Report the malaria status of this cell.
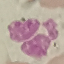

Uninfected.

Cell patch, automatically extracted from a larger field of view and resized to 64 × 64 pixels. Thin blood smear. Acquired by smartphone through the microscope eyepiece. Giemsa stain.